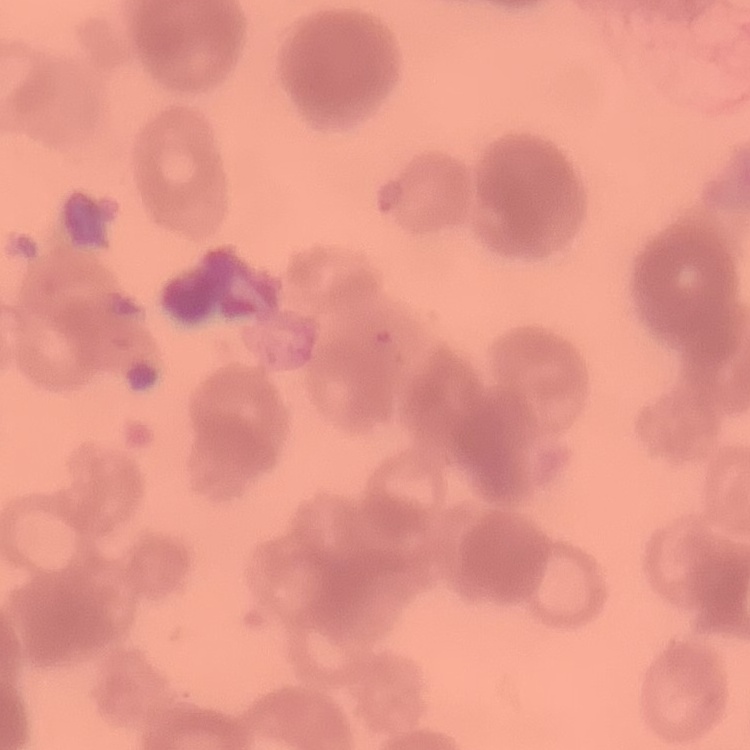
The erythrocytes exhibit rouleaux formation. Thin peripheral smear. Stained with either Field's or Giemsa. One tile cut from a larger photomicrograph.